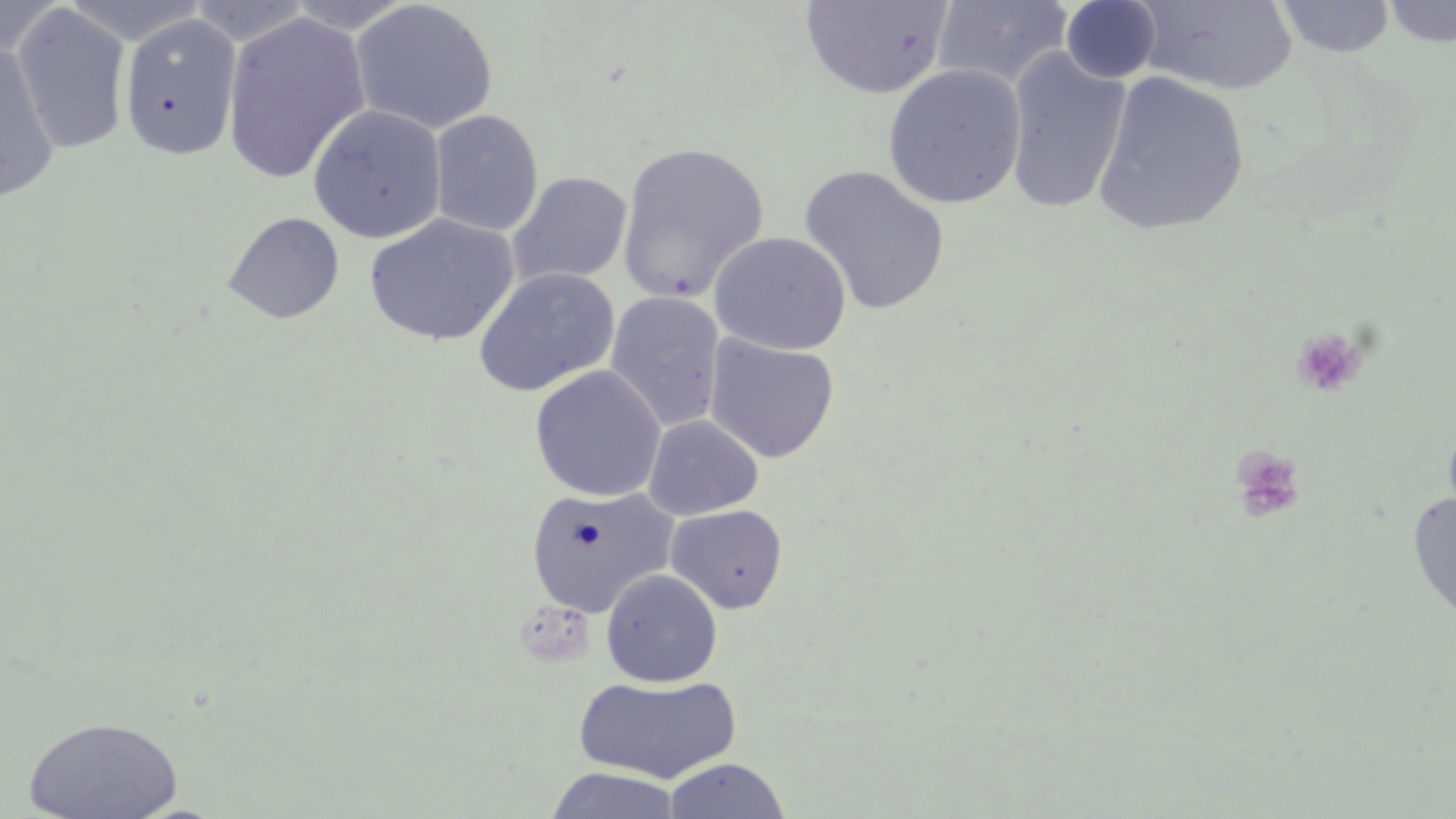

slide-level diagnosis = no evidence of blood parasites
field of view = single
modality = optical microscopy
uninfected red blood cell locations = approximate bounding boxes as named x1/y1/x2/y2 corners in pixels: (x1=0, y1=0, x2=66, y2=64), (x1=283, y1=0, x2=420, y2=34), (x1=348, y1=0, x2=499, y2=134), (x1=1060, y1=0, x2=1163, y2=84), (x1=1274, y1=0, x2=1396, y2=58), (x1=800, y1=1, x2=954, y2=99), (x1=932, y1=1, x2=1075, y2=90), (x1=1133, y1=1, x2=1297, y2=96), (x1=1381, y1=1, x2=1456, y2=47), (x1=189, y1=2, x2=315, y2=46), (x1=10, y1=4, x2=132, y2=155), (x1=220, y1=9, x2=371, y2=185), (x1=119, y1=13, x2=242, y2=161), (x1=0, y1=42, x2=60, y2=205), (x1=1003, y1=46, x2=1131, y2=215), (x1=882, y1=63, x2=1027, y2=210), (x1=1092, y1=69, x2=1250, y2=237), (x1=308, y1=105, x2=446, y2=243), (x1=429, y1=110, x2=544, y2=236), (x1=617, y1=142, x2=769, y2=302), (x1=798, y1=164, x2=950, y2=316), (x1=507, y1=171, x2=633, y2=288), (x1=222, y1=211, x2=345, y2=324), (x1=363, y1=213, x2=519, y2=347), (x1=710, y1=231, x2=851, y2=355), (x1=473, y1=267, x2=621, y2=396), (x1=605, y1=291, x2=726, y2=431), (x1=704, y1=333, x2=840, y2=464), (x1=529, y1=365, x2=666, y2=502), (x1=643, y1=415, x2=763, y2=520), (x1=652, y1=415, x2=774, y2=620), (x1=526, y1=485, x2=677, y2=618), (x1=1407, y1=489, x2=1456, y2=625), (x1=666, y1=504, x2=788, y2=614), (x1=601, y1=569, x2=723, y2=687), (x1=573, y1=674, x2=742, y2=784), (x1=23, y1=716, x2=183, y2=819), (x1=663, y1=757, x2=790, y2=819), (x1=545, y1=767, x2=681, y2=819)
image size = 1456×819 pixels
platelet locations = approximate bounding boxes as named x1/y1/x2/y2 corners in pixels: (x1=1291, y1=326, x2=1368, y2=399), (x1=1229, y1=446, x2=1306, y2=524)
preparation = thin blood smear
magnification = 1000x
stain = May-Grünwald-Giemsa